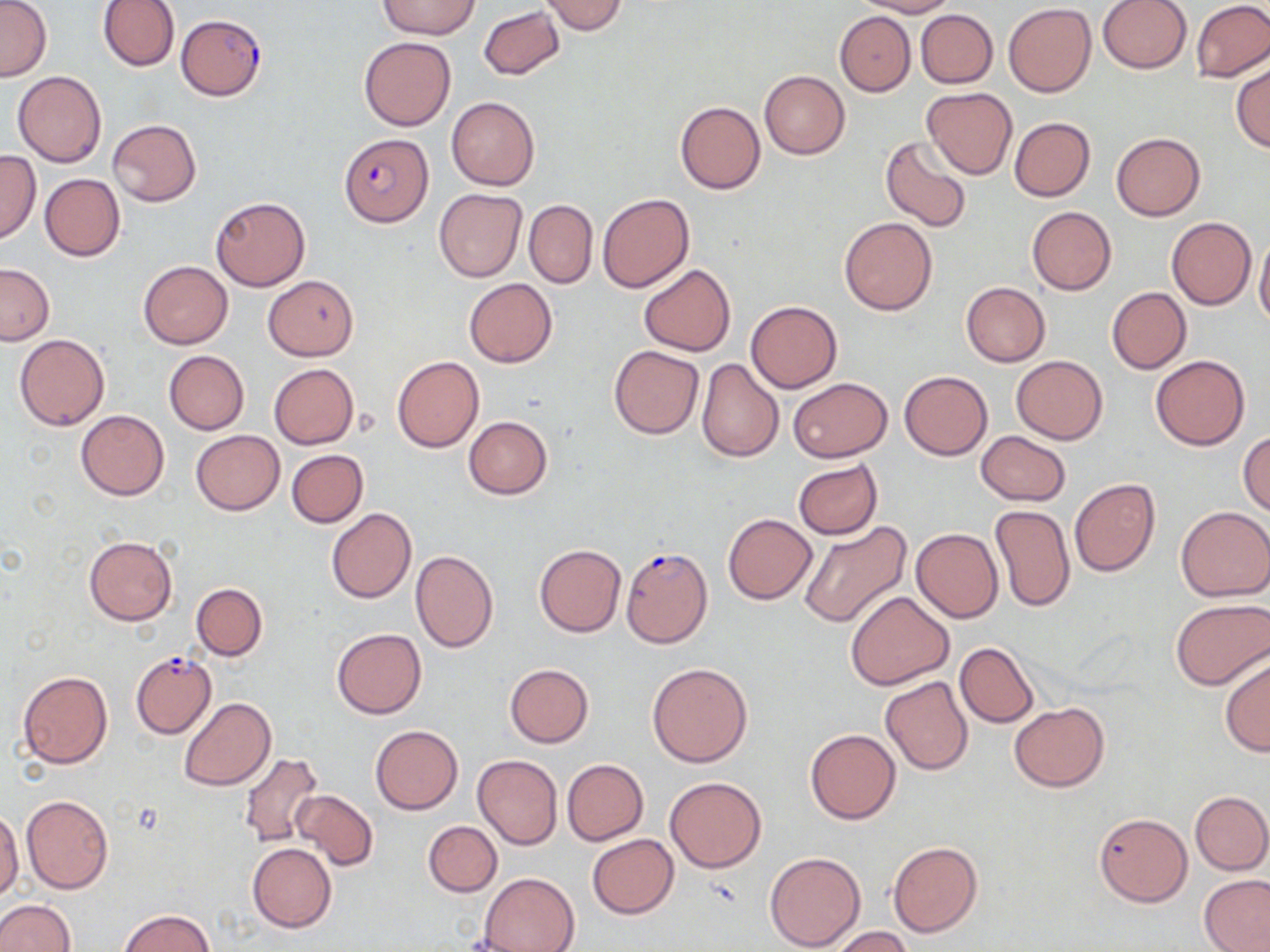
slide-level diagnosis = Plasmodium falciparum
uninfected red blood cell locations = approximate bounding boxes as named x1/y1/x2/y2 corners in pixels: (x1=0, y1=0, x2=51, y2=81), (x1=98, y1=0, x2=179, y2=71), (x1=379, y1=0, x2=480, y2=39), (x1=859, y1=0, x2=957, y2=17), (x1=1099, y1=0, x2=1191, y2=73), (x1=539, y1=1, x2=629, y2=35), (x1=1191, y1=1, x2=1270, y2=82), (x1=1003, y1=3, x2=1095, y2=96), (x1=478, y1=5, x2=564, y2=80), (x1=916, y1=9, x2=997, y2=88), (x1=835, y1=11, x2=915, y2=96), (x1=359, y1=36, x2=457, y2=131), (x1=1232, y1=61, x2=1270, y2=152), (x1=759, y1=70, x2=849, y2=159), (x1=12, y1=71, x2=107, y2=167), (x1=922, y1=87, x2=1016, y2=178), (x1=446, y1=96, x2=539, y2=191), (x1=675, y1=101, x2=765, y2=195), (x1=1009, y1=117, x2=1095, y2=201), (x1=107, y1=120, x2=202, y2=206), (x1=1111, y1=132, x2=1205, y2=220), (x1=880, y1=136, x2=974, y2=233), (x1=0, y1=150, x2=41, y2=243), (x1=40, y1=173, x2=125, y2=261), (x1=434, y1=188, x2=527, y2=281), (x1=597, y1=193, x2=693, y2=292), (x1=211, y1=197, x2=310, y2=291), (x1=523, y1=200, x2=598, y2=288), (x1=1026, y1=206, x2=1117, y2=294), (x1=1167, y1=216, x2=1256, y2=310), (x1=838, y1=217, x2=937, y2=315), (x1=1254, y1=230, x2=1270, y2=330), (x1=138, y1=261, x2=233, y2=348), (x1=0, y1=263, x2=54, y2=344), (x1=639, y1=264, x2=736, y2=356), (x1=263, y1=276, x2=359, y2=360), (x1=464, y1=278, x2=557, y2=367), (x1=960, y1=282, x2=1050, y2=365), (x1=1106, y1=287, x2=1191, y2=374), (x1=745, y1=300, x2=842, y2=392), (x1=14, y1=334, x2=109, y2=431), (x1=609, y1=345, x2=704, y2=439), (x1=164, y1=351, x2=249, y2=435), (x1=1151, y1=354, x2=1249, y2=450), (x1=392, y1=355, x2=484, y2=452), (x1=1011, y1=355, x2=1108, y2=444), (x1=695, y1=357, x2=783, y2=462), (x1=268, y1=363, x2=360, y2=449), (x1=899, y1=371, x2=993, y2=460), (x1=788, y1=377, x2=891, y2=462), (x1=76, y1=409, x2=169, y2=500), (x1=464, y1=416, x2=552, y2=498), (x1=190, y1=430, x2=285, y2=515), (x1=974, y1=430, x2=1072, y2=506), (x1=1238, y1=431, x2=1270, y2=516), (x1=287, y1=449, x2=368, y2=527), (x1=792, y1=459, x2=882, y2=540), (x1=1069, y1=478, x2=1160, y2=577), (x1=989, y1=504, x2=1075, y2=612), (x1=1176, y1=505, x2=1270, y2=601), (x1=326, y1=507, x2=416, y2=604), (x1=722, y1=513, x2=817, y2=604), (x1=797, y1=520, x2=911, y2=629), (x1=911, y1=527, x2=1003, y2=623), (x1=83, y1=536, x2=177, y2=626), (x1=534, y1=544, x2=626, y2=637), (x1=409, y1=549, x2=497, y2=652), (x1=191, y1=582, x2=267, y2=660), (x1=844, y1=590, x2=954, y2=690), (x1=1169, y1=599, x2=1269, y2=690), (x1=332, y1=628, x2=425, y2=719), (x1=956, y1=641, x2=1039, y2=727), (x1=1219, y1=654, x2=1270, y2=756), (x1=647, y1=662, x2=752, y2=767), (x1=505, y1=663, x2=594, y2=746), (x1=18, y1=671, x2=113, y2=769), (x1=881, y1=676, x2=973, y2=775), (x1=178, y1=697, x2=275, y2=791), (x1=1008, y1=702, x2=1110, y2=791), (x1=370, y1=724, x2=463, y2=815), (x1=805, y1=728, x2=901, y2=824), (x1=238, y1=753, x2=325, y2=849), (x1=472, y1=754, x2=563, y2=850), (x1=561, y1=758, x2=649, y2=846), (x1=664, y1=776, x2=766, y2=873), (x1=291, y1=790, x2=377, y2=870), (x1=1190, y1=791, x2=1270, y2=874), (x1=21, y1=795, x2=113, y2=895), (x1=0, y1=808, x2=24, y2=901), (x1=1094, y1=812, x2=1192, y2=906), (x1=423, y1=820, x2=502, y2=895), (x1=587, y1=835, x2=679, y2=919), (x1=887, y1=841, x2=983, y2=936), (x1=246, y1=842, x2=336, y2=932), (x1=764, y1=850, x2=867, y2=951), (x1=480, y1=873, x2=579, y2=952), (x1=1199, y1=873, x2=1270, y2=952), (x1=0, y1=899, x2=75, y2=952), (x1=118, y1=910, x2=216, y2=952), (x1=831, y1=927, x2=914, y2=952)
stain = May-Grünwald-Giemsa
image size = 1270×952 pixels
Plasmodium falciparum-infected red blood cell locations = approximate bounding boxes as named x1/y1/x2/y2 corners in pixels: (x1=176, y1=13, x2=267, y2=101), (x1=338, y1=133, x2=431, y2=227), (x1=620, y1=545, x2=713, y2=648), (x1=131, y1=652, x2=217, y2=739)
preparation = thin blood film
magnification = 1000x
modality = optical microscopy
field of view = single